Assess this cell for malaria.
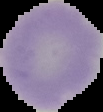
It is uninfected.

image_size: 103×112 pixels
image_type: segmented cell region with the area outside set to black
preparation: thin blood film